Report the malaria status of this cell.
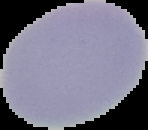

Uninfected.

Image is 148×130 pixels. Segmented cell region on a black background. From a thin blood smear.